Give the preparation type.
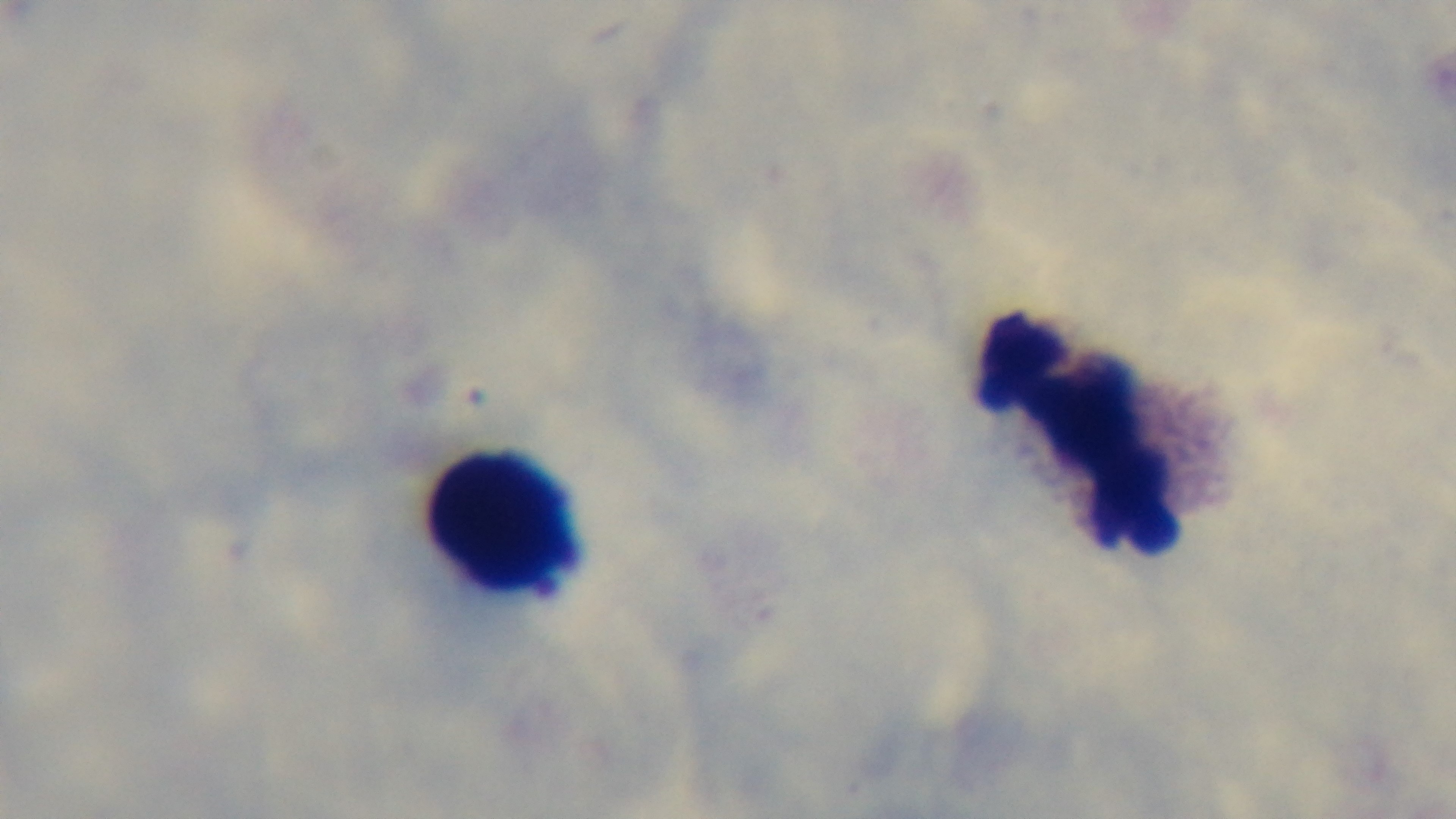

Thick.

{
  "capture": "mounted 4K digital camera",
  "stain": "Giemsa",
  "malaria_status": "uninfected",
  "field_of_view": "single",
  "objective": "100x oil immersion",
  "modality": "light microscopy"
}